Assess this cell for malaria.
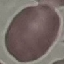
Uninfected.

image type = cell patch, automatically extracted from a larger field of view and resized to 64 × 64 pixels
preparation = thin blood smear
capture = smartphone camera at the microscope eyepiece
stain = Giemsa